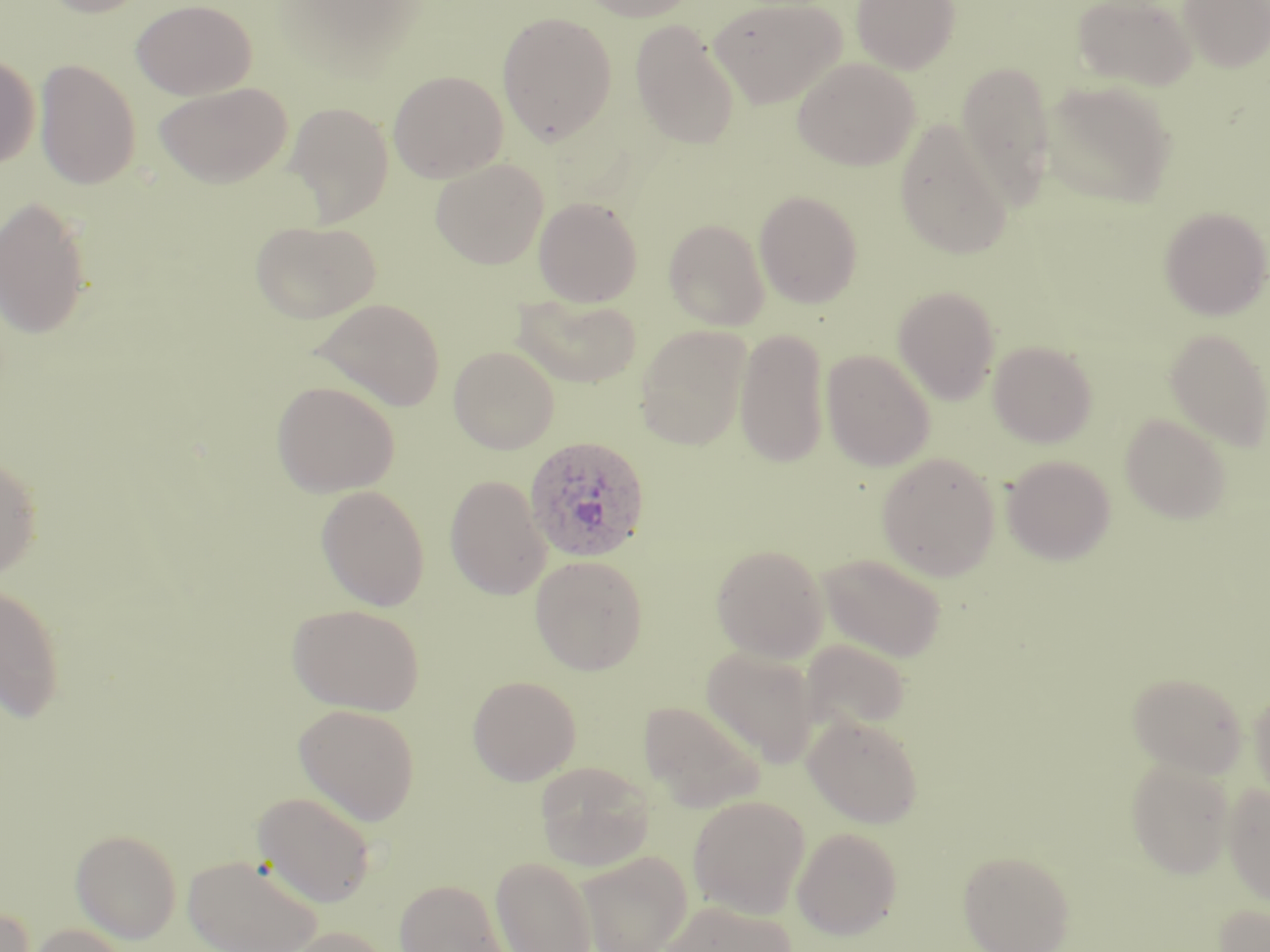
{
  "plasmodium_ovale_infected_red_blood_cell_locations": "approximate bounding boxes as named x1/y1/x2/y2 corners in pixels: (x1=523, y1=435, x2=651, y2=562)",
  "slide_level_diagnosis": "Plasmodium ovale",
  "uninfected_red_blood_cell_locations": "approximate bounding boxes as named x1/y1/x2/y2 corners in pixels: (x1=39, y1=0, x2=155, y2=17), (x1=131, y1=0, x2=256, y2=100), (x1=578, y1=0, x2=699, y2=22), (x1=709, y1=0, x2=846, y2=108), (x1=851, y1=0, x2=960, y2=74), (x1=1073, y1=0, x2=1198, y2=91), (x1=1179, y1=0, x2=1270, y2=73), (x1=497, y1=12, x2=617, y2=144), (x1=630, y1=20, x2=741, y2=150), (x1=0, y1=54, x2=40, y2=169), (x1=792, y1=57, x2=920, y2=171), (x1=35, y1=59, x2=141, y2=189), (x1=956, y1=60, x2=1057, y2=209), (x1=388, y1=69, x2=508, y2=182), (x1=153, y1=81, x2=292, y2=188), (x1=1041, y1=81, x2=1176, y2=208), (x1=284, y1=100, x2=394, y2=227), (x1=894, y1=119, x2=1013, y2=260), (x1=430, y1=158, x2=549, y2=269), (x1=754, y1=190, x2=864, y2=308), (x1=0, y1=196, x2=93, y2=340), (x1=533, y1=196, x2=643, y2=307), (x1=1159, y1=206, x2=1269, y2=320), (x1=664, y1=218, x2=769, y2=330), (x1=249, y1=220, x2=381, y2=323), (x1=893, y1=286, x2=1001, y2=403), (x1=513, y1=294, x2=642, y2=388), (x1=311, y1=297, x2=446, y2=411), (x1=635, y1=325, x2=751, y2=450), (x1=734, y1=328, x2=831, y2=468), (x1=1164, y1=328, x2=1269, y2=450), (x1=988, y1=340, x2=1098, y2=447), (x1=448, y1=345, x2=559, y2=454), (x1=821, y1=349, x2=935, y2=471), (x1=270, y1=380, x2=401, y2=497), (x1=1120, y1=413, x2=1232, y2=523), (x1=876, y1=451, x2=1001, y2=580), (x1=0, y1=455, x2=42, y2=579), (x1=1002, y1=455, x2=1116, y2=565), (x1=445, y1=474, x2=551, y2=600), (x1=315, y1=484, x2=430, y2=611), (x1=711, y1=543, x2=829, y2=662), (x1=818, y1=552, x2=946, y2=661), (x1=529, y1=554, x2=648, y2=675), (x1=0, y1=583, x2=66, y2=722), (x1=287, y1=603, x2=424, y2=715), (x1=801, y1=639, x2=910, y2=732), (x1=701, y1=646, x2=819, y2=765), (x1=1128, y1=672, x2=1248, y2=778), (x1=467, y1=675, x2=581, y2=785), (x1=1249, y1=686, x2=1270, y2=804), (x1=639, y1=701, x2=765, y2=812), (x1=293, y1=702, x2=421, y2=825), (x1=803, y1=714, x2=923, y2=828), (x1=1126, y1=758, x2=1235, y2=878), (x1=535, y1=761, x2=654, y2=871), (x1=1223, y1=783, x2=1270, y2=906), (x1=252, y1=791, x2=377, y2=908), (x1=688, y1=795, x2=809, y2=918), (x1=792, y1=827, x2=902, y2=940), (x1=71, y1=829, x2=182, y2=944), (x1=957, y1=849, x2=1075, y2=952), (x1=576, y1=850, x2=693, y2=952), (x1=183, y1=853, x2=323, y2=952), (x1=491, y1=855, x2=598, y2=952), (x1=394, y1=878, x2=508, y2=952), (x1=657, y1=901, x2=797, y2=952), (x1=1211, y1=901, x2=1270, y2=952), (x1=0, y1=906, x2=36, y2=952), (x1=29, y1=923, x2=129, y2=952), (x1=279, y1=925, x2=392, y2=952)",
  "field_of_view": "one of a larger specimen",
  "stain": "May-Grünwald-Giemsa",
  "magnification": "1000x",
  "preparation": "thin blood smear",
  "modality": "optical microscopy",
  "image_size": "1270×952 pixels"
}